Assess the morphology of the erythrocytes.
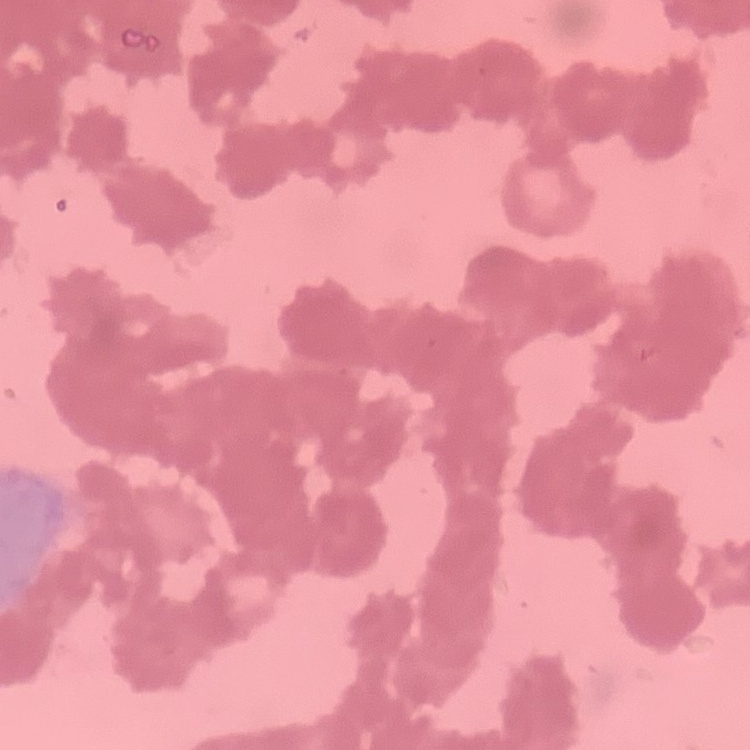
Rouleaux formation.

Summary:
  - Preparation: thin blood smear
  - Image type: square crop of a larger photomicrograph
  - Stain: Field's or Giemsa